Describe the morphology of the red blood cells.
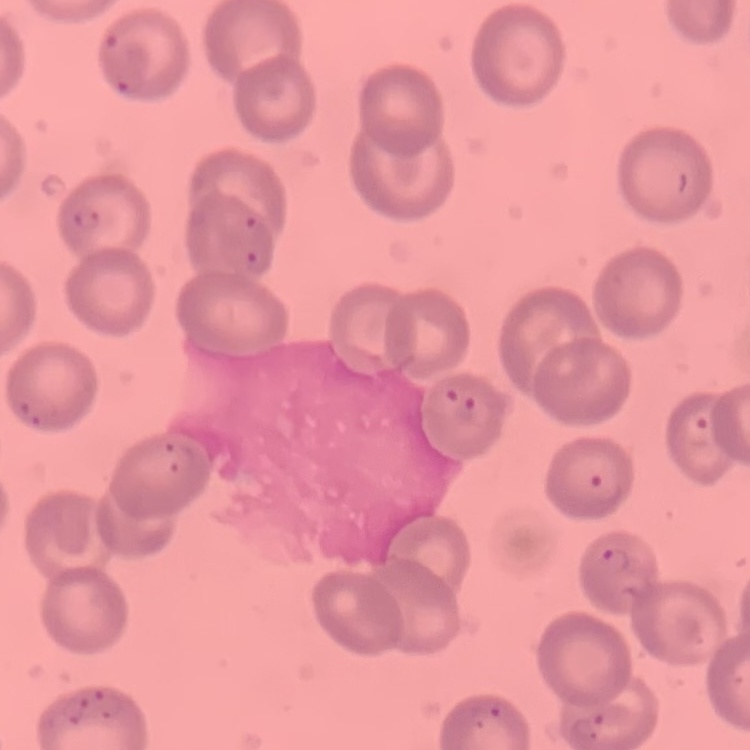

No rouleaux formation.

Summary:
  - Preparation: thin blood smear
  - Stain: Field's or Giemsa
  - Image type: one tile cut from a larger photomicrograph